Give the position of every leukocyte.
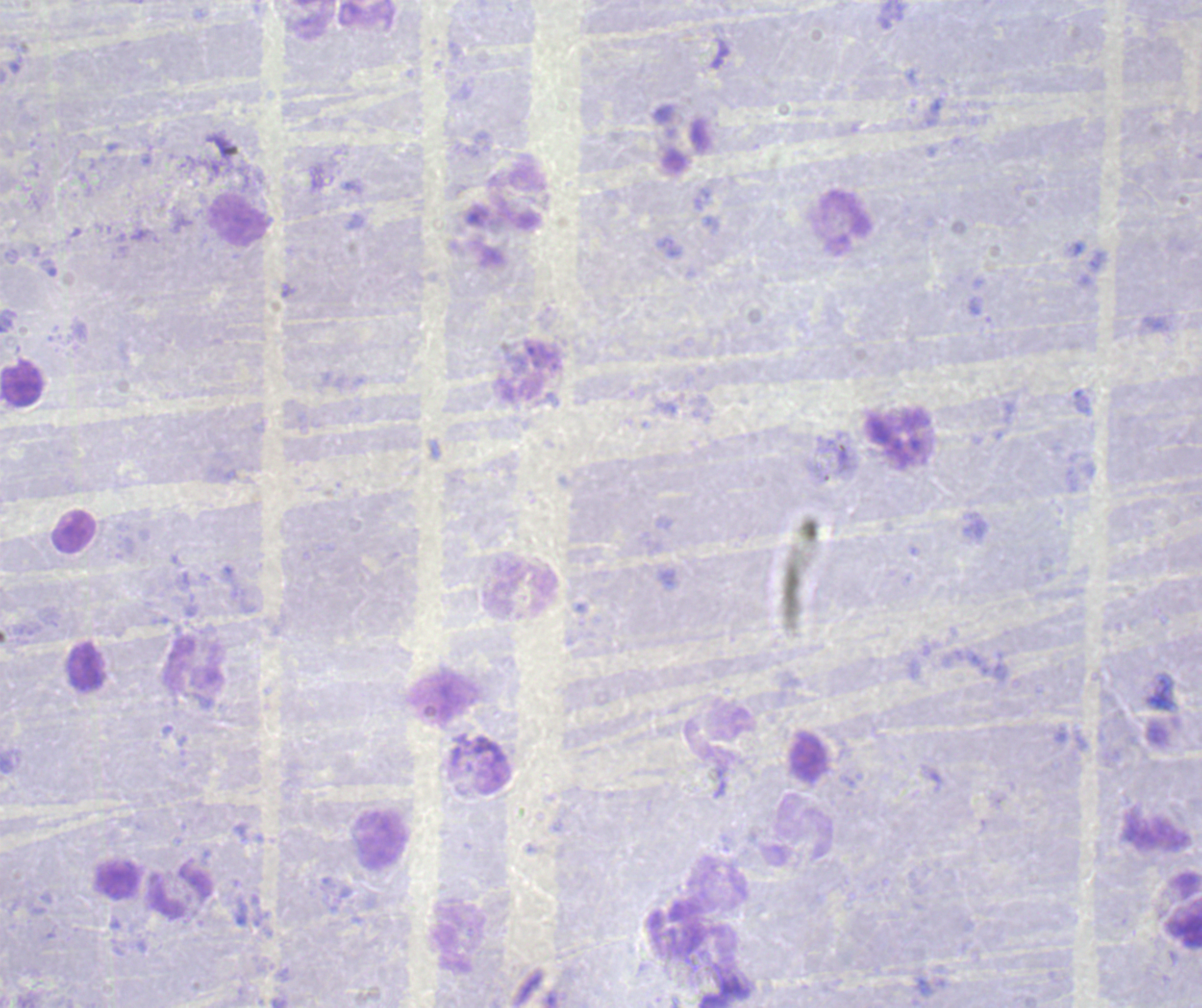

Approximate object centers, in pixels from the top-left corner.
Leukocytes: (x=682, y=138), (x=515, y=200), (x=238, y=221), (x=21, y=384), (x=73, y=531), (x=520, y=589), (x=798, y=829), (x=381, y=838), (x=179, y=892), (x=1183, y=912).

Summary:
  - Background quality: poor
  - Context: previously used in a real diagnosis
  - Image size: 1202×1008 pixels
  - Magnification: 100x
  - Field of view: single
  - Result: no malaria parasites detected
  - Stain: Romanowsky
  - Preparation: thick smear of blood